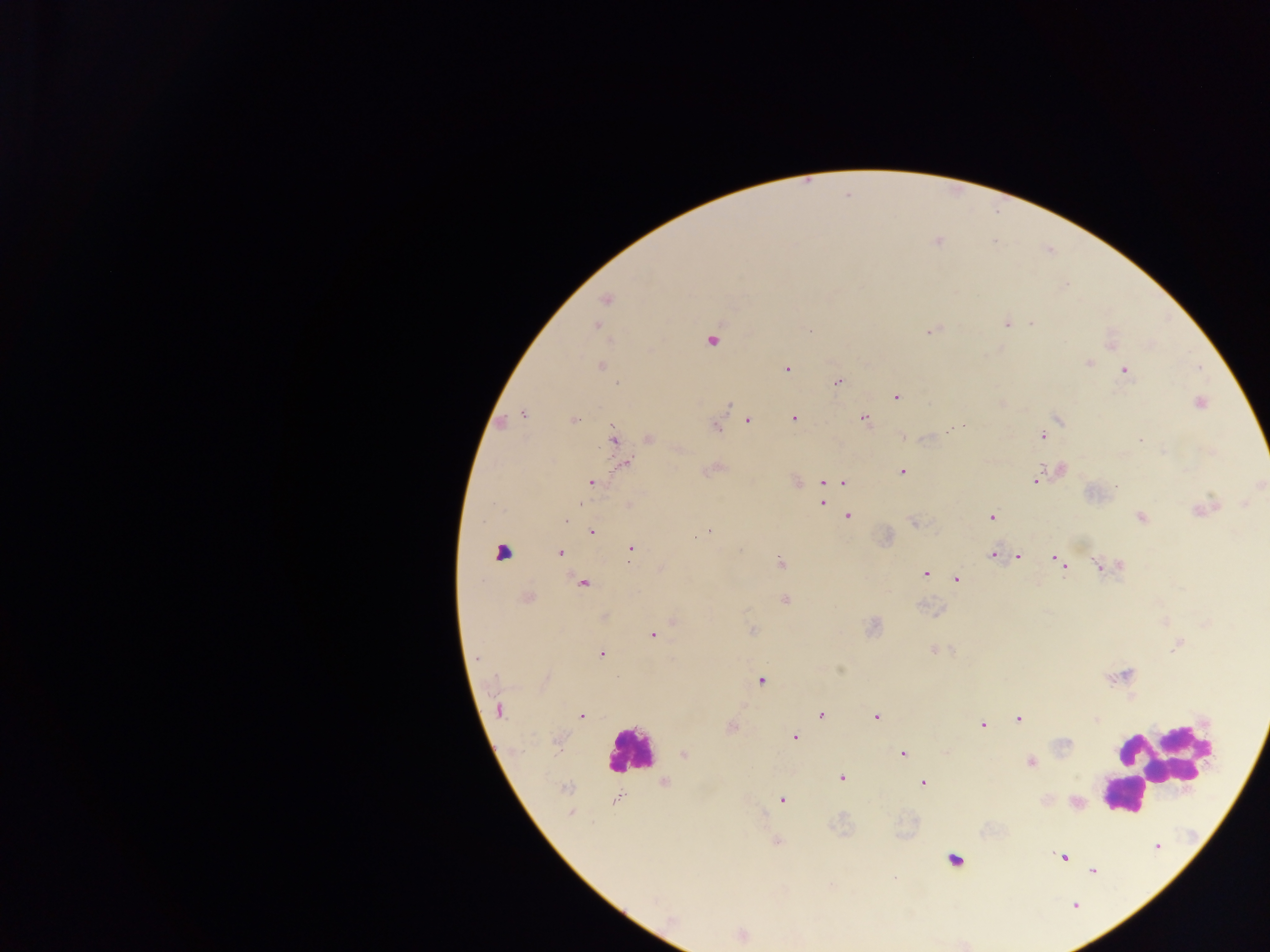
Approximate centers as [x, y] in pixels.
Summary:
  - Malaria parasite locations: [606, 299], [1007, 323], [1031, 323], [597, 325], [931, 330], [711, 340], [1110, 342], [1088, 362], [600, 365], [787, 368], [1123, 370], [837, 382], [896, 397], [1199, 402], [523, 414], [793, 417], [863, 417], [1057, 417], [574, 420], [746, 420], [500, 422], [716, 425], [1042, 435], [613, 438], [648, 438], [624, 464], [712, 468], [1060, 469], [901, 471], [1036, 481], [591, 482], [796, 482], [843, 482], [822, 483], [830, 483], [821, 502], [628, 505], [1202, 508], [848, 515], [1140, 516], [990, 517], [915, 522], [592, 532], [709, 532], [630, 549], [501, 552], [560, 552], [992, 554], [1018, 557], [1054, 558], [779, 562], [1062, 565], [1098, 565], [1119, 566], [925, 573], [956, 579], [582, 583], [526, 597], [784, 600], [605, 616], [673, 621], [751, 629], [653, 635], [1178, 643], [933, 649], [600, 653], [760, 680], [499, 709], [822, 715], [581, 716], [877, 717], [1019, 718], [1096, 719], [981, 724], [731, 726], [794, 736], [903, 753], [684, 754], [1030, 761], [842, 778], [664, 782], [924, 782], [565, 788], [782, 799], [617, 800], [1076, 803], [571, 813], [776, 842], [1156, 846], [1063, 857], [1091, 870], [740, 935]
  - Leukocyte locations: [630, 750], [1170, 752], [1162, 765], [1123, 796], [951, 866]
  - Preparation: thick blood film
  - Country: Ghana
  - Capture: mobile-phone photograph through a microscope
  - Field of view: single
  - Image size: 1270×952 pixels